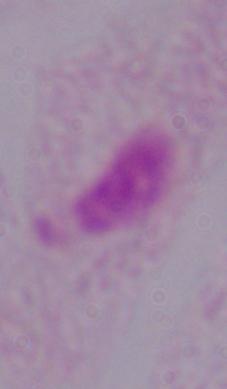

modality = micrograph
magnification = 1000x
identification = trichomonad